Locate every blood parasite and identify its species.
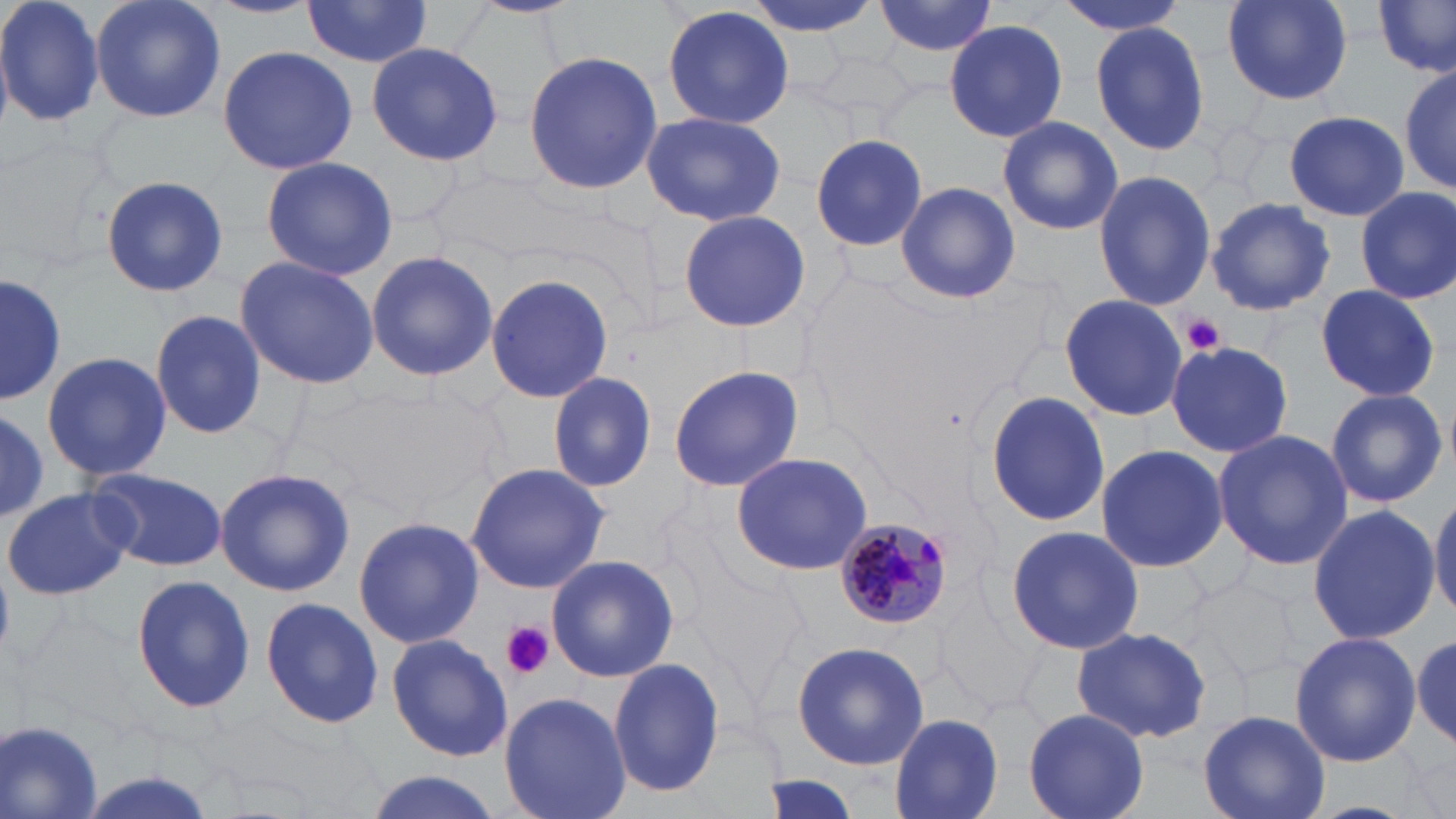
Approximate bounding boxes as (x1,y1)-(x2,y2) corner pairs in pixels.
Plasmodium malariae-infected red blood cells: (835,518)-(955,628).
No Plasmodium falciparum, Plasmodium ovale, Plasmodium vivax, Babesia divergens, or Trypanosoma brucei observed.

slide_level_diagnosis: Plasmodium malariae
stain: May-Grünwald-Giemsa
platelet_locations: 'approximate bounding boxes as (x1,y1)-(x2,y2) corner pairs in pixels: (1183,314)-(1228,354), (499,621)-(555,680)'
preparation: thin blood film
field_of_view: one of a larger specimen
modality: light microscopy
magnification: 1000x
uninfected_red_blood_cell_locations: 'approximate bounding boxes as (x1,y1)-(x2,y2) corner pairs in pixels: (0,0)-(105,130), (87,0)-(226,124), (204,0)-(319,19), (740,0)-(886,39), (874,0)-(997,57), (1055,0)-(1189,36), (1217,0)-(1357,105), (1373,1)-(1455,79), (299,2)-(436,67), (662,4)-(796,130), (945,20)-(1067,141), (1090,24)-(1211,157), (366,41)-(503,168), (216,45)-(358,176), (520,49)-(664,197), (1399,60)-(1454,200), (641,111)-(787,228), (1284,111)-(1410,221), (997,116)-(1123,237), (806,132)-(930,254), (259,156)-(400,282), (430,169)-(561,262), (1093,169)-(1216,311), (100,175)-(227,296), (895,181)-(1020,304), (1354,187)-(1455,305), (1206,197)-(1337,315), (678,210)-(812,332), (364,248)-(501,384), (233,255)-(379,391), (0,271)-(63,409), (486,273)-(614,404), (1313,284)-(1441,400), (1059,294)-(1188,423), (151,312)-(266,442), (1167,341)-(1291,458), (40,349)-(171,484), (667,365)-(805,492), (547,371)-(657,493), (329,383)-(503,515), (1324,388)-(1451,508), (984,389)-(1109,528), (0,409)-(49,518), (1212,429)-(1354,571), (1094,445)-(1228,574), (731,452)-(876,575), (465,462)-(610,595), (214,464)-(355,599), (86,467)-(227,571), (3,486)-(133,601), (1431,489)-(1456,624), (1307,503)-(1439,646), (352,516)-(483,650), (1005,525)-(1144,653), (546,554)-(679,686), (130,574)-(256,713), (1193,580)-(1296,686), (259,597)-(385,731), (1070,626)-(1212,744), (1288,632)-(1424,766), (1410,632)-(1456,751), (386,633)-(515,761), (792,640)-(930,770), (607,658)-(726,797), (497,690)-(630,819), (1023,707)-(1149,819), (1199,708)-(1331,819), (889,713)-(1005,819), (1,717)-(105,819), (358,769)-(509,819), (757,775)-(867,817)'
image_size: 1456×819 pixels